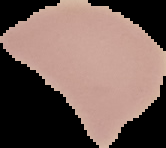

Summary:
  - Preparation: thin blood film
  - Image size: 166×148 pixels
  - Result: no malaria parasites detected
  - Image type: cell region segmented out of the field of view; surrounding area masked to black